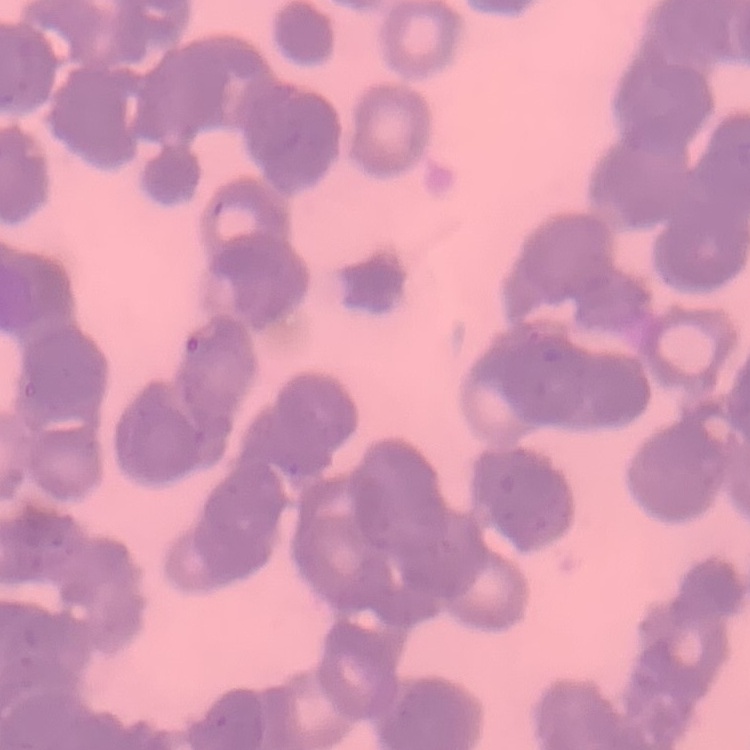

erythrocyte morphology = rouleaux formation
stain = Field's or Giemsa
preparation = thin blood smear
image type = one tile cut from a larger photomicrograph